Outline each uninfected red blood cell.
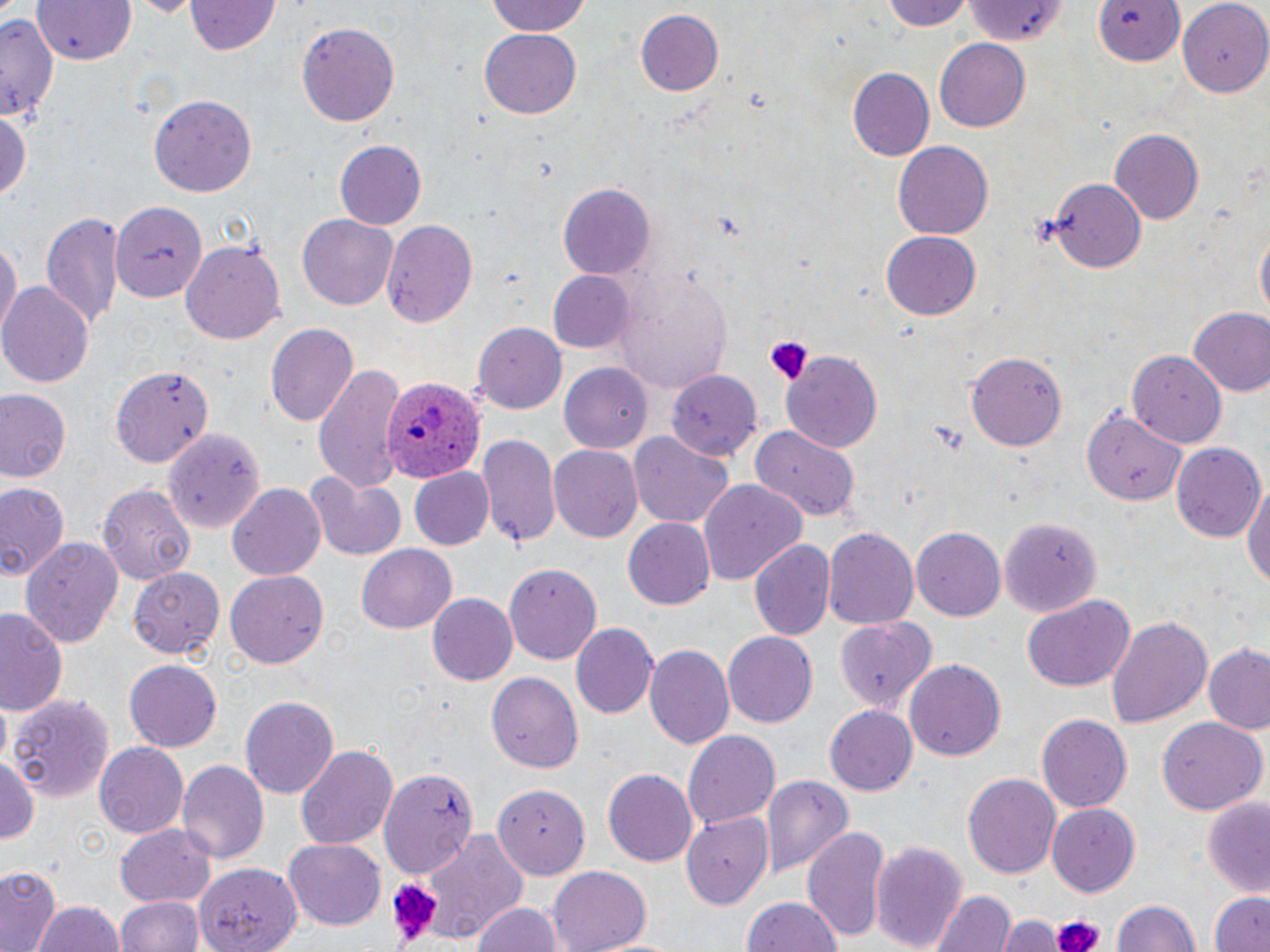

Approximate bounding boxes as (x1,y1)-(x2,y2) corner pairs in pixels.
Uninfected red blood cells: (128,0)-(203,17), (481,0)-(596,38), (882,0)-(976,30), (1092,1)-(1189,71), (35,2)-(137,65), (187,2)-(281,56), (1179,2)-(1270,96), (962,3)-(1068,48), (634,9)-(723,97), (0,13)-(59,118), (295,21)-(403,129), (480,30)-(580,118), (935,39)-(1031,132), (849,68)-(934,160), (150,93)-(257,196), (0,107)-(32,205), (1110,130)-(1203,222), (894,139)-(992,236), (333,140)-(426,228), (1051,177)-(1146,271), (559,183)-(655,282), (111,201)-(208,303), (41,210)-(124,331), (296,212)-(400,311), (381,219)-(480,327), (1254,228)-(1269,325), (881,231)-(982,319), (0,238)-(19,338), (180,240)-(286,345), (548,270)-(635,353), (615,273)-(732,393), (1,282)-(94,387), (1186,305)-(1270,397), (471,321)-(565,412), (264,322)-(357,427), (780,351)-(883,454), (964,351)-(1068,452), (1127,351)-(1226,447), (312,363)-(405,489), (560,363)-(656,453), (111,364)-(215,468), (660,371)-(762,458), (0,387)-(71,485), (1084,406)-(1191,505), (162,427)-(265,533), (749,427)-(860,524), (475,432)-(561,548), (629,433)-(734,530), (1170,443)-(1264,542), (549,444)-(642,540), (408,468)-(494,551), (306,472)-(407,561), (1241,474)-(1270,598), (0,479)-(68,585), (700,481)-(809,587), (98,483)-(196,584), (229,484)-(326,581), (997,515)-(1101,617), (623,519)-(715,609), (824,526)-(920,630), (912,527)-(1006,621), (750,538)-(835,640), (21,539)-(121,646), (357,542)-(457,632), (505,562)-(600,667), (226,567)-(329,665), (129,568)-(225,657), (426,594)-(518,685), (1023,595)-(1134,691), (0,607)-(66,716), (1107,614)-(1213,728), (836,617)-(938,713), (571,624)-(656,718), (722,632)-(817,728), (645,645)-(735,751), (1204,646)-(1270,734), (124,659)-(222,752), (905,659)-(1007,764), (486,671)-(583,773), (7,694)-(116,804), (241,695)-(339,799), (824,704)-(919,796), (1036,714)-(1132,812), (1158,718)-(1267,814), (682,730)-(780,830), (94,744)-(189,839), (295,745)-(399,851), (0,756)-(39,847), (176,759)-(269,864), (604,767)-(700,867), (378,768)-(479,876), (961,771)-(1061,878), (760,775)-(853,877), (495,782)-(593,878), (1201,798)-(1270,896), (1047,804)-(1140,896), (682,810)-(774,909), (803,824)-(887,941), (115,826)-(215,911), (417,829)-(528,948), (284,840)-(387,930), (869,840)-(968,952), (0,866)-(60,950), (545,866)-(651,951), (932,889)-(1015,952), (1212,891)-(1270,952), (118,895)-(202,952), (740,897)-(843,952), (1112,900)-(1202,951), (471,901)-(564,952), (33,902)-(127,952), (999,916)-(1060,952).

Summary:
  - Plasmodium ovale-infected red blood cell locations: (382,377)-(484,482)
  - Platelet locations: (764,336)-(813,385), (927,422)-(968,453), (383,878)-(445,947), (1048,911)-(1107,952)
  - Slide-level diagnosis: Plasmodium ovale
  - Image size: 1270×952 pixels
  - Modality: optical microscopy
  - Stain: May-Grünwald-Giemsa
  - Preparation: thin blood smear
  - Magnification: 1000x
  - Field of view: one of a larger specimen